Assess this cell for malaria.
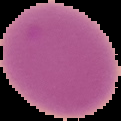

Uninfected.

Summary:
  - Preparation: thin blood film
  - Image size: 121×121 pixels
  - Image type: segmented cell region with the area outside set to black